Name the parasite shown.
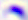
Toxoplasma gondii.

Photomicrograph. Captured at 400x magnification.